Assess this cell for malaria.
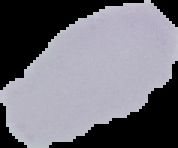
Uninfected.

From a thin blood film. Image is 178×148 pixels. The area outside the segmented cell region is set to black.